Report the malaria status of this cell.
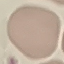
It is uninfected.

Summary:
  - Capture: smartphone through the microscope eyepiece
  - Preparation: thin smear
  - Stain: Giemsa
  - Image type: cell patch, automatically extracted from a larger field of view and resized to 64 × 64 pixels